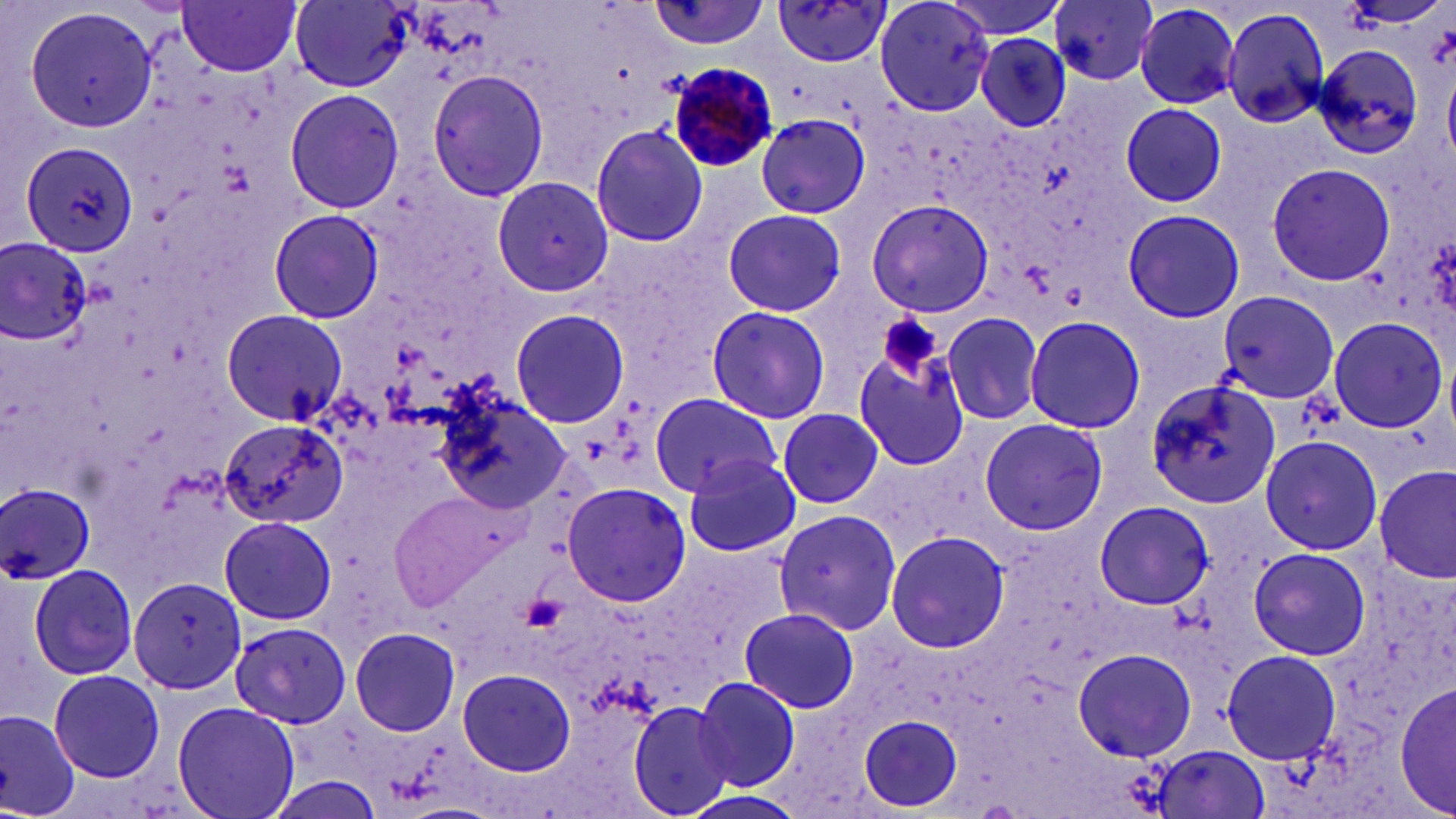

Summary:
  - Coordinate format: approximate bounding boxes as (x1,y1)-(x2,y2) corner pairs in pixels
  - Uninfected red blood cell locations: (646,0)-(770,50), (771,0)-(893,69), (871,0)-(995,116), (939,0)-(1073,40), (1050,0)-(1159,85), (178,1)-(301,76), (291,1)-(414,91), (16,4)-(159,137), (1135,4)-(1240,108), (1219,6)-(1333,130), (976,35)-(1072,133), (1310,41)-(1427,161), (423,69)-(549,203), (427,71)-(551,201), (285,89)-(404,212), (1121,102)-(1227,207), (755,112)-(870,218), (589,123)-(708,246), (21,142)-(142,256), (1265,161)-(1396,286), (493,178)-(615,297), (865,199)-(995,321), (268,208)-(386,324), (1123,208)-(1244,323), (723,209)-(845,316), (1,236)-(92,348), (1214,291)-(1339,403), (706,305)-(831,424), (221,308)-(346,424), (509,308)-(630,428), (942,310)-(1046,424), (1023,314)-(1146,433), (1328,316)-(1449,432), (854,341)-(970,471), (1146,378)-(1283,511), (650,388)-(784,495), (435,389)-(573,513), (650,396)-(787,497), (777,408)-(882,509), (979,416)-(1107,535), (218,419)-(344,531), (1259,434)-(1384,555), (682,453)-(802,557), (1374,465)-(1455,585), (0,480)-(98,586), (562,483)-(692,607), (389,485)-(520,607), (1093,500)-(1210,610), (773,507)-(903,636), (219,515)-(337,626), (886,530)-(1010,654), (1248,546)-(1371,661), (26,562)-(139,681), (129,577)-(246,695), (739,608)-(861,713), (228,623)-(353,725), (351,627)-(460,737), (1222,645)-(1344,772), (1075,647)-(1200,766), (1072,649)-(1198,763), (49,668)-(164,782), (458,668)-(574,776), (693,676)-(800,790), (1394,677)-(1455,816), (173,700)-(301,819), (627,700)-(735,816), (0,708)-(81,817), (860,714)-(962,813), (1145,744)-(1269,819), (260,776)-(388,819), (674,789)-(811,819)
  - Platelet locations: (1424,23)-(1456,70), (877,314)-(940,381)
  - Plasmodium malariae-infected red blood cell locations: (667,61)-(779,171)
  - Slide-level diagnosis: Plasmodium malariae
  - Image size: 1456×819 pixels
  - Modality: optical microscopy
  - Preparation: thin blood smear
  - Field of view: one of a larger specimen
  - Stain: May-Grünwald-Giemsa
  - Magnification: 1000x